State which parasite is depicted.
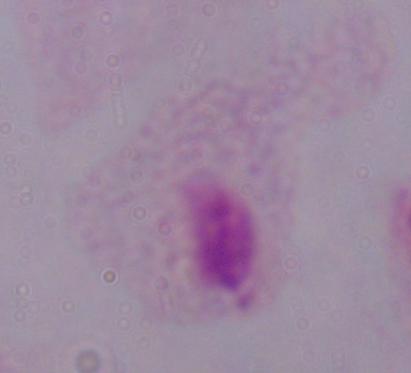
A trichomonad.

Summary:
  - Modality: micrograph
  - Magnification: 1000x